Describe the morphology of the red blood cells.
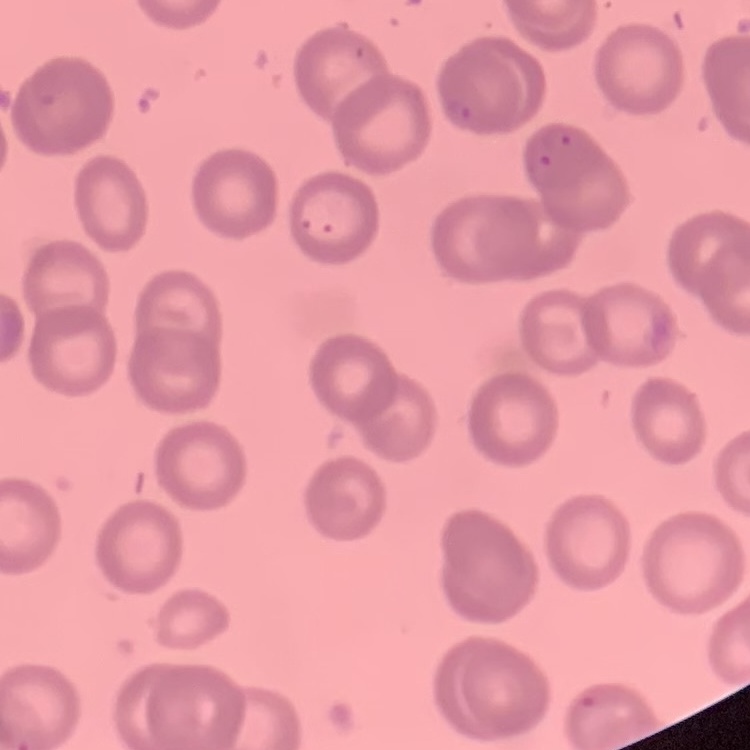
No rouleaux formation.

Summary:
  - Stain: Field's or Giemsa
  - Image type: one tile cut from a larger photomicrograph
  - Preparation: thin blood smear